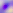
Summary:
  - Identification: Toxoplasma gondii
  - Modality: photomicrograph
  - Magnification: 400x